State which parasite is depicted.
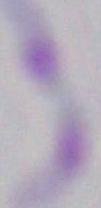

Toxoplasma gondii.

Photomicrograph. 1000x magnification.